Describe the morphology of the red blood cells.
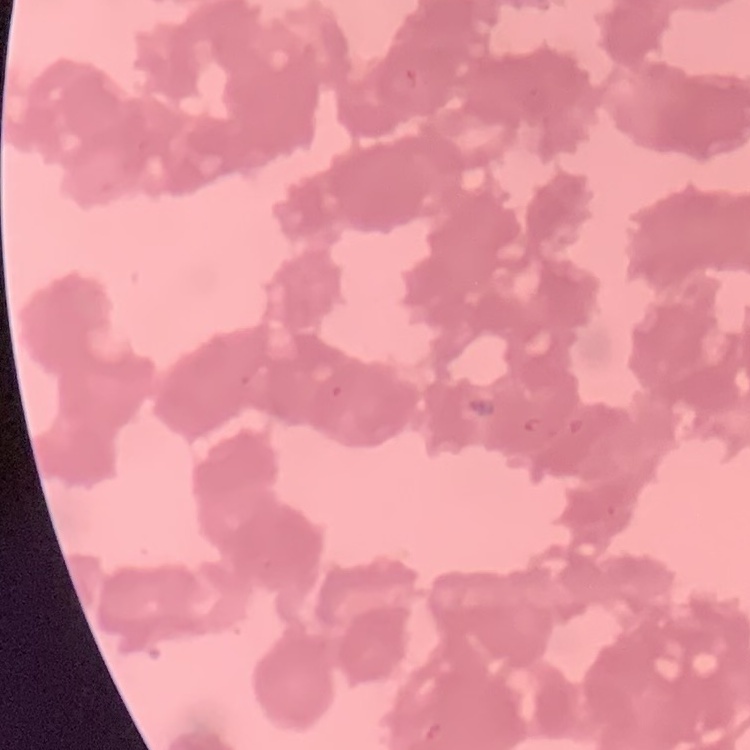
They show rouleaux formation.

Thin blood smear. Square crop of a larger photomicrograph. Field's or Giemsa stain.